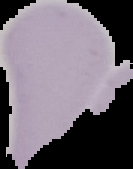

{
  "malaria_status": "uninfected",
  "preparation": "thin blood film",
  "image_type": "segmented cell region on a black background",
  "image_size": "133×169 pixels"
}